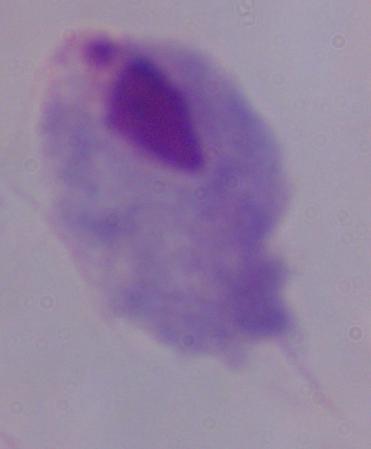

Summary:
  - Modality: photomicrograph
  - Magnification: 1000x
  - Identification: trichomonad